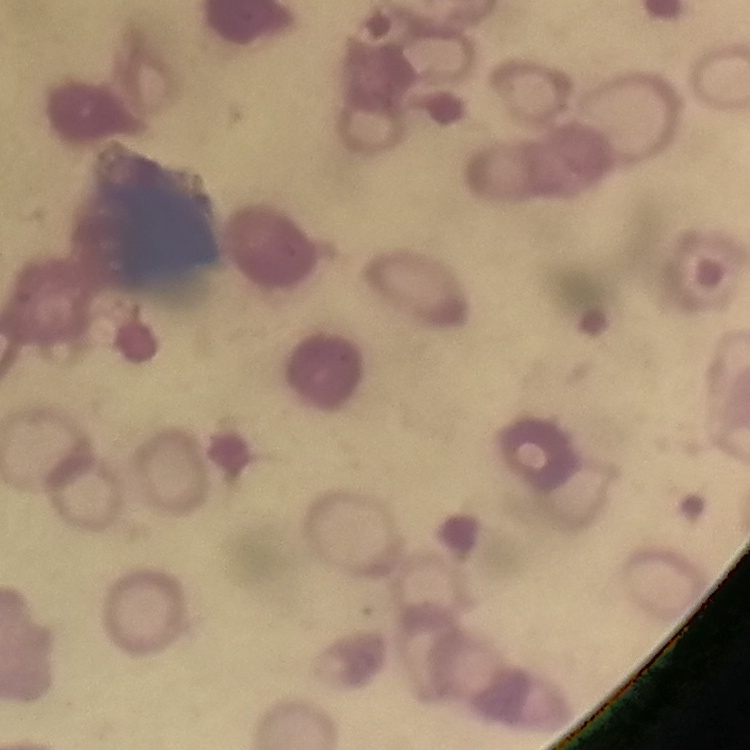
Summary:
  - Red blood cell morphology: rouleaux formation
  - Preparation: thin blood film
  - Image type: square crop of a larger photomicrograph
  - Stain: Field's or Giemsa